Name the parasite shown.
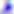

This is Toxoplasma gondii.

modality = photomicrograph
magnification = 400x